Classify this cell by malaria status.
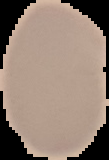
Uninfected.

Segmented cell region on a black background. From a thin blood smear. Image is 109×160 pixels.